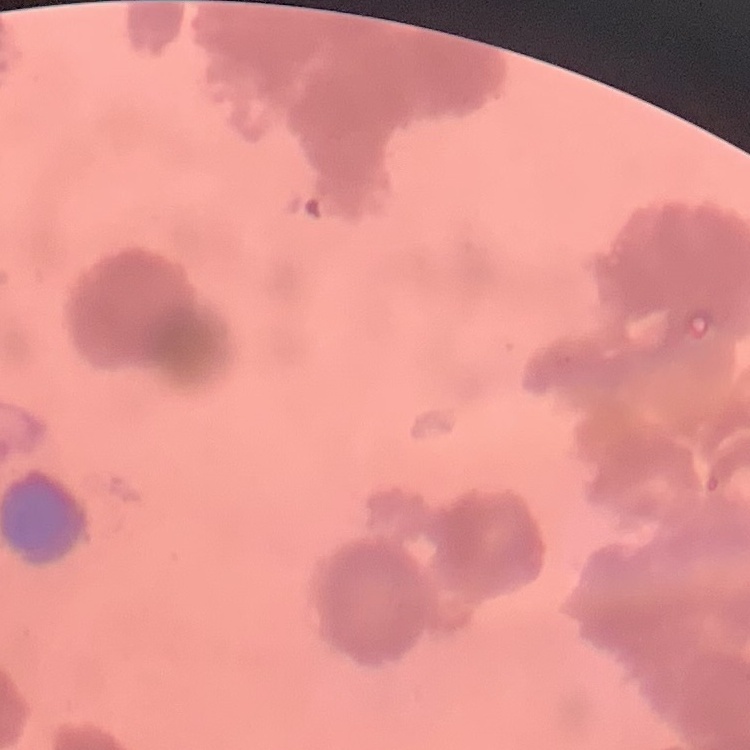

The red blood cells show rouleaux formation. Thin blood film. One tile cut from a larger photomicrograph. Field's or Giemsa stain.